Outline each Babesia divergens-infected red blood cell.
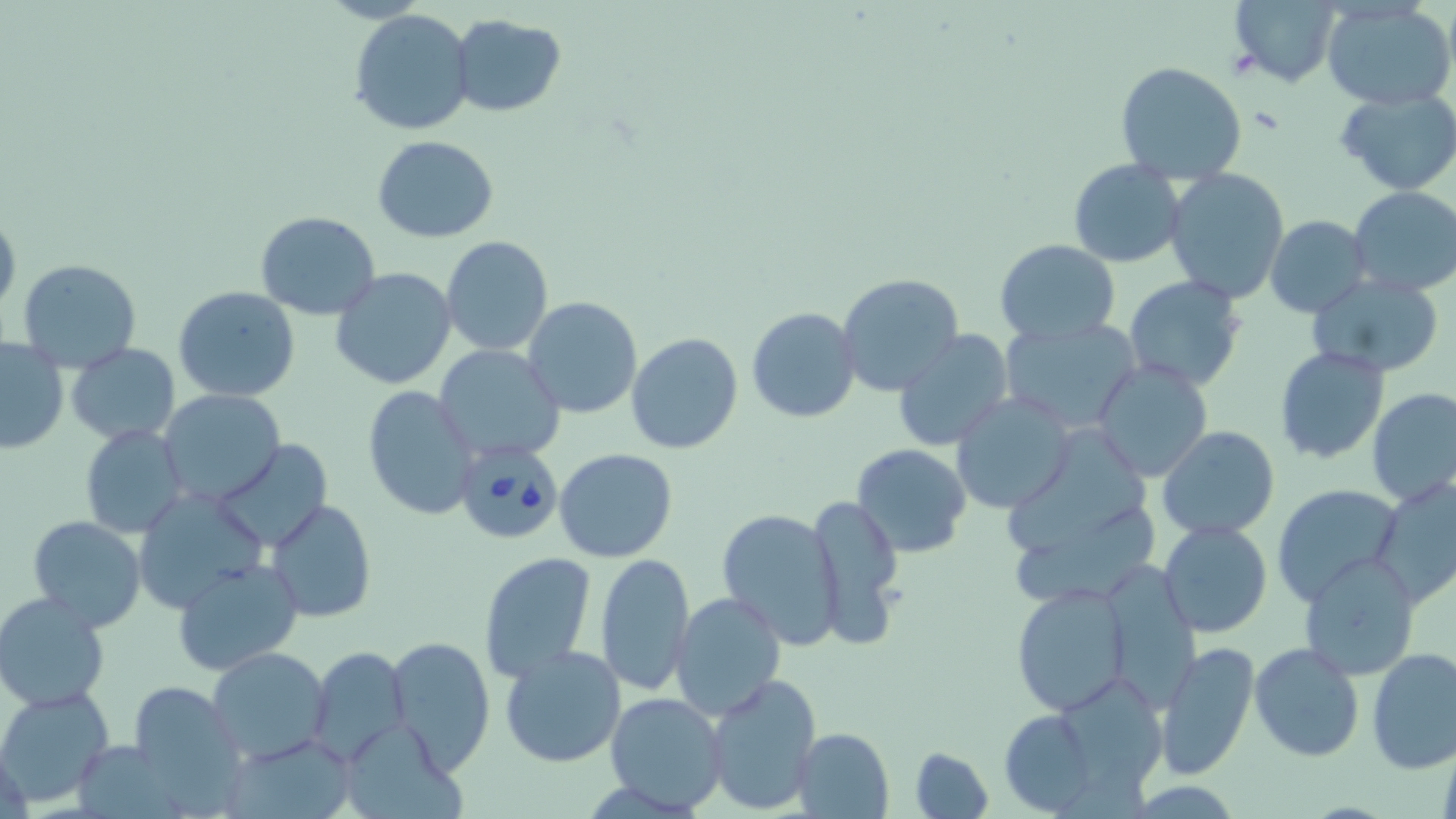

Approximate bounding boxes as (x1,y1)-(x2,y2) corner pairs in pixels.
Babesia divergens-infected red blood cells: (454,438)-(563,545).

slide-level diagnosis = Babesia divergens
stain = May-Grünwald-Giemsa
modality = light microscopy
magnification = 1000x
uninfected red blood cell locations = approximate bounding boxes as (x1,y1)-(x2,y2) corner pairs in pixels: (1231,1)-(1340,86), (1322,3)-(1454,111), (349,9)-(475,136), (449,14)-(565,116), (1115,60)-(1249,186), (1336,88)-(1455,196), (371,135)-(499,241), (1067,159)-(1185,267), (1164,167)-(1290,303), (1347,185)-(1456,298), (0,206)-(21,322), (256,211)-(381,319), (1265,215)-(1371,318), (440,237)-(553,356), (995,239)-(1121,345), (15,258)-(142,373), (330,266)-(457,390), (835,273)-(964,396), (1305,273)-(1444,379), (1123,274)-(1248,392), (174,285)-(302,403), (521,296)-(643,419), (747,307)-(861,423), (999,316)-(1141,434), (453,317)-(629,443), (893,330)-(1015,450), (626,332)-(744,455), (0,337)-(69,454), (64,343)-(181,442), (432,344)-(565,463), (1274,345)-(1392,465), (1093,360)-(1213,482), (363,385)-(482,521), (1366,389)-(1456,510), (159,390)-(286,504), (951,393)-(1072,514), (80,423)-(190,541), (1002,423)-(1152,550), (1157,426)-(1279,539), (214,439)-(333,550), (852,444)-(972,558), (554,449)-(678,563), (1372,475)-(1456,606), (1271,483)-(1401,604), (131,486)-(270,615), (804,491)-(904,649), (266,499)-(377,623), (1014,504)-(1166,598), (718,507)-(845,648), (26,516)-(149,632), (1158,520)-(1272,638), (477,550)-(597,683), (594,553)-(695,697), (1299,553)-(1422,678), (172,557)-(304,675), (1110,561)-(1201,710), (1009,582)-(1134,713), (670,591)-(786,722), (0,592)-(115,712), (387,635)-(496,774), (1153,640)-(1260,779), (1248,641)-(1365,764), (499,644)-(629,768), (207,647)-(334,765), (306,647)-(410,765), (1365,648)-(1456,773), (702,673)-(821,816), (1067,677)-(1171,800), (127,681)-(251,812), (0,687)-(115,806), (603,690)-(728,812), (998,710)-(1099,813), (791,727)-(894,819), (348,728)-(473,818), (228,736)-(355,818), (908,746)-(993,819)
image size = 1456×819 pixels
field of view = one of a larger specimen
preparation = thin blood smear